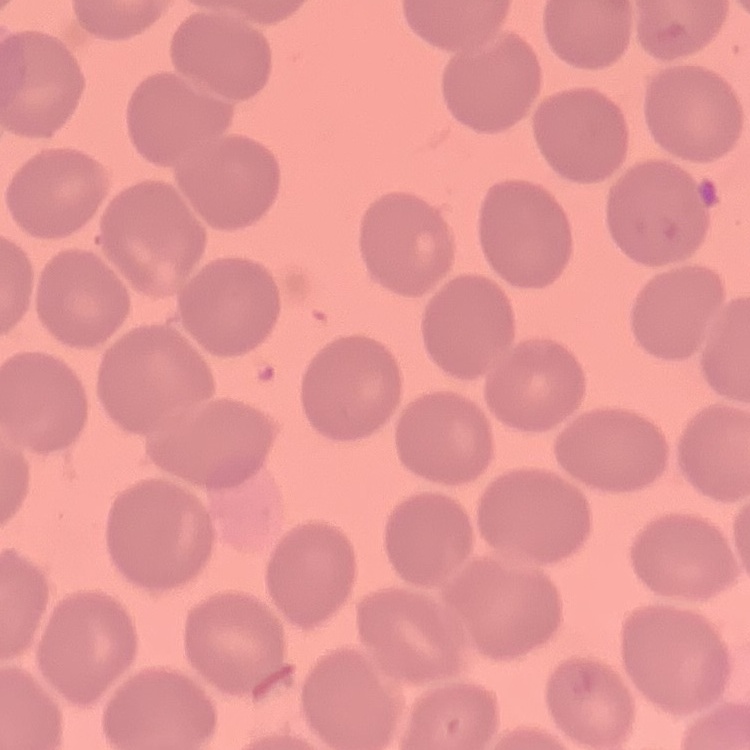 The red blood cells exhibit no rouleaux formation. One tile cut from a larger photomicrograph. Field's or Giemsa stain. Thin blood smear.